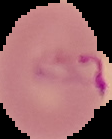
Summary:
  - Malaria status: parasitized
  - Preparation: thin blood smear
  - Image size: 112×139 pixels
  - Image type: segmented cell region with the area outside set to black